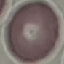
Malaria status: uninfected. Automatically extracted cell patch, resized to 64 × 64 pixels. Acquired by smartphone through the microscope eyepiece. Thin blood film. Giemsa stain.